Classify this cell by malaria status.
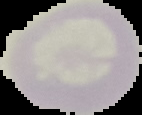

It is uninfected.

Image is 142×115 pixels. From a thin blood smear. The area outside the segmented cell region is set to black.